Report the malaria status of this cell.
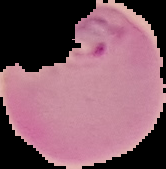

Parasitized.

Summary:
  - Image size: 166×169 pixels
  - Preparation: thin blood film
  - Image type: segmented cell region with the area outside set to black